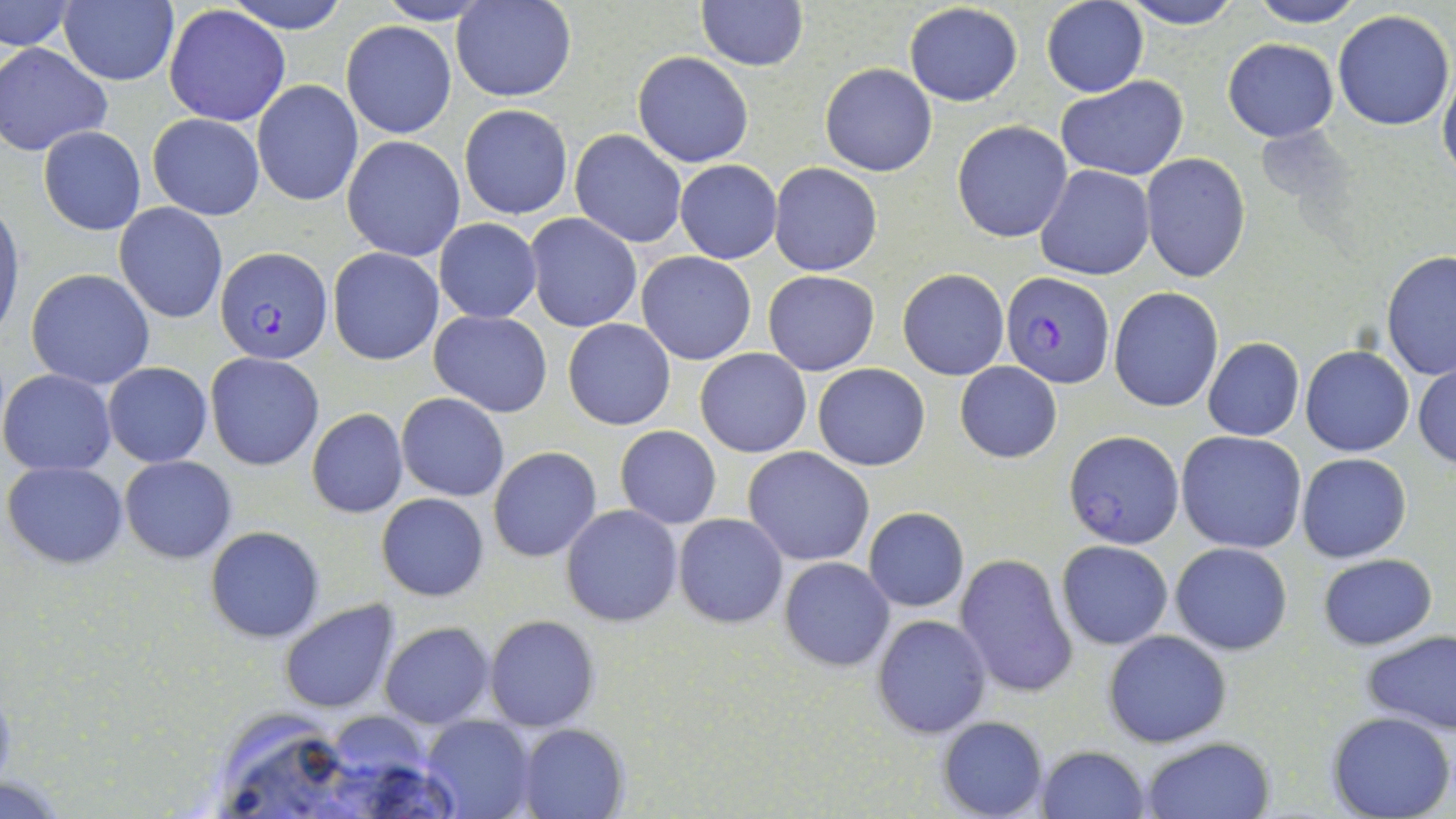

slide_level_diagnosis: Plasmodium falciparum
stain: May-Grünwald-Giemsa
preparation: thin blood smear
field_of_view: one of a larger specimen
plasmodium_falciparum_infected_red_blood_cell_locations: 'approximate bounding boxes as (x1,y1)-(x2,y2) corner pairs in pixels: (216,247)-(332,366), (1000,270)-(1116,390), (1064,431)-(1184,548)'
uninfected_red_blood_cell_locations: 'approximate bounding boxes as (x1,y1)-(x2,y2) corner pairs in pixels: (222,0)-(352,32), (372,0)-(496,25), (453,0)-(576,101), (1042,0)-(1147,97), (1121,0)-(1242,29), (1249,0)-(1367,27), (695,1)-(808,71), (1,2)-(75,50), (59,2)-(178,86), (903,3)-(1024,106), (164,5)-(290,128), (663,5)-(798,116), (1331,9)-(1454,130), (342,21)-(457,138), (1223,38)-(1338,142), (1,42)-(112,157), (633,52)-(753,167), (820,62)-(937,176), (1439,71)-(1456,184), (1056,75)-(1190,181), (251,80)-(363,206), (458,104)-(573,220), (147,113)-(265,220), (951,120)-(1072,242), (38,126)-(146,235), (569,130)-(688,247), (342,135)-(466,262), (1141,153)-(1251,281), (675,159)-(781,264), (770,162)-(882,276), (1035,165)-(1155,281), (0,201)-(24,343), (114,204)-(228,323), (524,213)-(642,333), (434,218)-(542,322), (328,248)-(444,364), (1381,250)-(1456,380), (636,251)-(757,365), (897,268)-(1009,380), (26,269)-(156,390), (763,270)-(880,377), (1109,286)-(1223,413), (429,310)-(551,418), (563,318)-(675,429), (1203,338)-(1305,441), (1301,345)-(1414,456), (695,348)-(811,459), (205,352)-(323,470), (955,361)-(1061,464), (1413,361)-(1456,470), (104,362)-(212,466), (812,362)-(930,471), (0,369)-(117,476), (397,393)-(509,500), (307,409)-(409,518), (614,426)-(721,528), (1176,431)-(1308,554), (488,446)-(602,562), (743,446)-(875,567), (1296,452)-(1412,563), (120,455)-(236,563), (4,461)-(128,567), (376,493)-(490,602), (561,504)-(684,627), (865,507)-(971,612), (673,512)-(788,629), (206,527)-(324,642), (1056,540)-(1173,649), (1170,540)-(1293,655), (954,552)-(1078,697), (1317,554)-(1438,649), (778,557)-(895,671), (1142,557)-(1273,710), (280,601)-(399,714), (484,614)-(600,733), (873,615)-(993,739), (380,622)-(494,730), (1103,629)-(1233,748), (1360,629)-(1456,737), (1326,709)-(1454,819), (422,713)-(536,818), (936,716)-(1049,819), (519,723)-(629,819), (1140,736)-(1276,819), (1035,746)-(1152,819), (0,777)-(69,817)'
modality: optical microscopy
magnification: 1000x
image_size: 1456×819 pixels